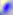
{
  "modality": "photomicrograph",
  "identification": "Toxoplasma gondii",
  "magnification": "400x"
}